Assess this cell for malaria.
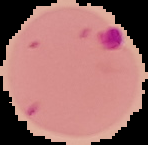
It is parasitized.

Summary:
  - Preparation: thin blood smear
  - Image type: cell region segmented out of the field of view; surrounding area masked to black
  - Image size: 148×145 pixels